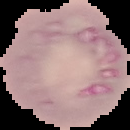
{
  "image_type": "segmented cell region on a black background",
  "malaria_status": "uninfected",
  "preparation": "thin blood smear",
  "image_size": "130×130 pixels"
}